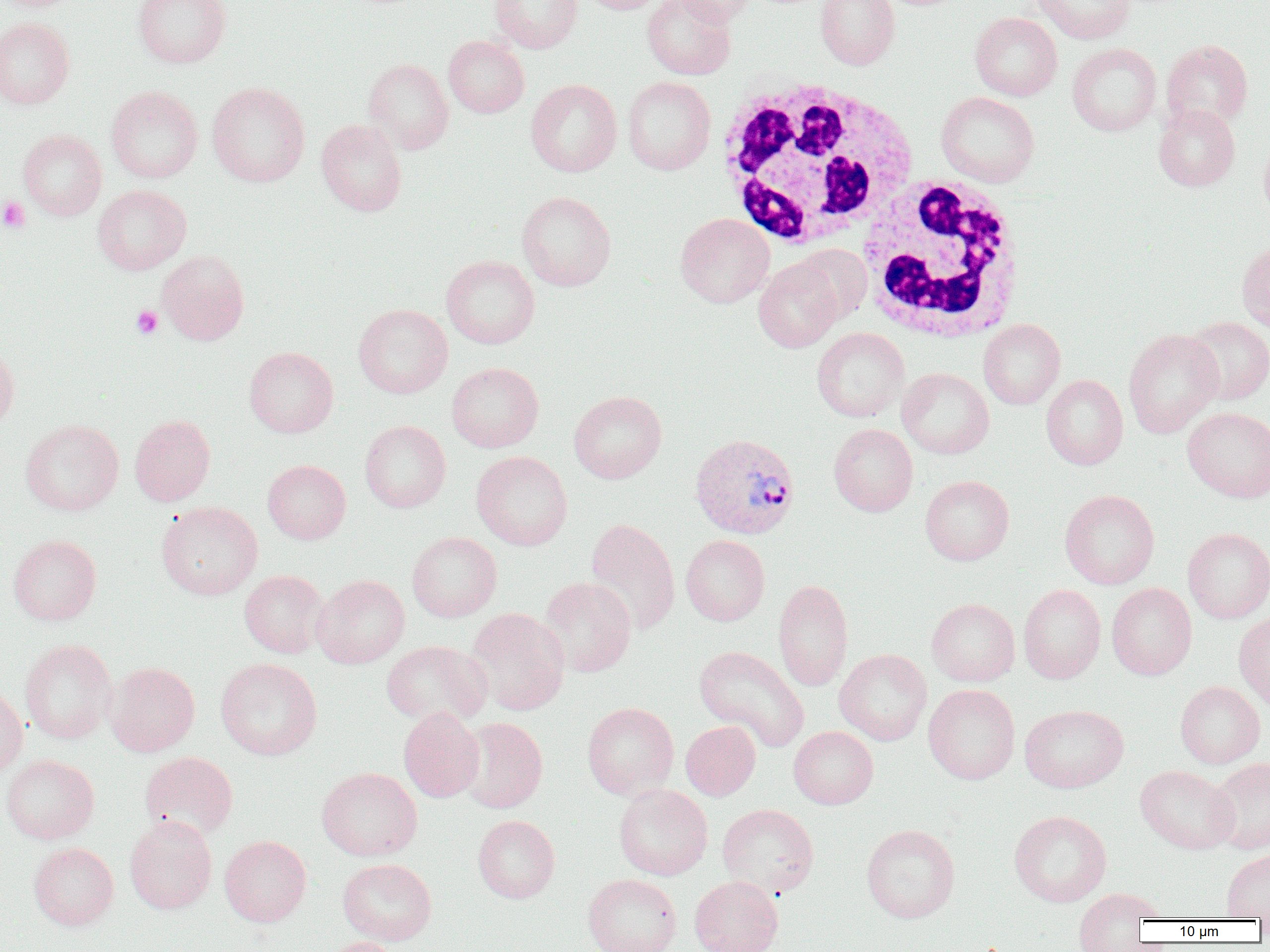

Summary:
  - Coordinate format: approximate bounding boxes as named x1/y1/x2/y2 corners in pixels
  - Platelet locations: (x1=0, y1=196, x2=31, y2=233), (x1=131, y1=305, x2=163, y2=339)
  - Plasmodium vivax-infected red blood cell locations: (x1=689, y1=433, x2=800, y2=539)
  - White blood cell locations: (x1=713, y1=77, x2=920, y2=249), (x1=855, y1=177, x2=1026, y2=343)
  - Uninfected red blood cell locations: (x1=133, y1=0, x2=231, y2=68), (x1=490, y1=0, x2=582, y2=53), (x1=579, y1=0, x2=667, y2=14), (x1=642, y1=0, x2=736, y2=80), (x1=672, y1=0, x2=757, y2=26), (x1=815, y1=0, x2=899, y2=70), (x1=1031, y1=0, x2=1134, y2=44), (x1=969, y1=12, x2=1062, y2=101), (x1=0, y1=18, x2=74, y2=109), (x1=443, y1=35, x2=529, y2=118), (x1=1161, y1=39, x2=1253, y2=131), (x1=1067, y1=43, x2=1162, y2=136), (x1=364, y1=58, x2=453, y2=154), (x1=622, y1=76, x2=716, y2=175), (x1=526, y1=79, x2=622, y2=177), (x1=207, y1=83, x2=310, y2=187), (x1=106, y1=86, x2=203, y2=183), (x1=936, y1=91, x2=1040, y2=187), (x1=1153, y1=103, x2=1240, y2=192), (x1=316, y1=119, x2=407, y2=216), (x1=18, y1=129, x2=106, y2=220), (x1=1258, y1=136, x2=1270, y2=222), (x1=92, y1=185, x2=191, y2=275), (x1=516, y1=191, x2=616, y2=291), (x1=675, y1=213, x2=774, y2=308), (x1=1237, y1=238, x2=1270, y2=334), (x1=793, y1=244, x2=872, y2=323), (x1=157, y1=250, x2=249, y2=345), (x1=441, y1=255, x2=539, y2=349), (x1=753, y1=258, x2=843, y2=352), (x1=353, y1=304, x2=452, y2=398), (x1=1183, y1=316, x2=1270, y2=405), (x1=978, y1=319, x2=1065, y2=409), (x1=812, y1=327, x2=909, y2=422), (x1=1123, y1=329, x2=1223, y2=438), (x1=0, y1=344, x2=19, y2=430), (x1=244, y1=346, x2=338, y2=437), (x1=446, y1=362, x2=544, y2=452), (x1=897, y1=367, x2=994, y2=459), (x1=1041, y1=375, x2=1128, y2=470), (x1=569, y1=390, x2=667, y2=484), (x1=1183, y1=407, x2=1270, y2=503), (x1=129, y1=414, x2=215, y2=506), (x1=20, y1=419, x2=123, y2=516), (x1=359, y1=421, x2=451, y2=513), (x1=829, y1=423, x2=918, y2=516), (x1=471, y1=451, x2=573, y2=550), (x1=262, y1=459, x2=351, y2=544), (x1=920, y1=475, x2=1014, y2=565), (x1=1059, y1=489, x2=1160, y2=589), (x1=155, y1=501, x2=262, y2=600), (x1=584, y1=518, x2=680, y2=635), (x1=1182, y1=528, x2=1270, y2=624), (x1=407, y1=531, x2=502, y2=622), (x1=8, y1=534, x2=101, y2=625), (x1=681, y1=535, x2=770, y2=626), (x1=239, y1=569, x2=328, y2=658), (x1=312, y1=574, x2=409, y2=668), (x1=539, y1=577, x2=636, y2=677), (x1=773, y1=579, x2=854, y2=691), (x1=1107, y1=583, x2=1197, y2=680), (x1=1018, y1=584, x2=1106, y2=684), (x1=926, y1=598, x2=1020, y2=686), (x1=466, y1=607, x2=569, y2=715), (x1=1234, y1=613, x2=1270, y2=712), (x1=20, y1=639, x2=117, y2=744), (x1=381, y1=640, x2=491, y2=727), (x1=694, y1=645, x2=809, y2=751), (x1=834, y1=649, x2=932, y2=745), (x1=215, y1=657, x2=322, y2=760), (x1=105, y1=662, x2=200, y2=756), (x1=1175, y1=681, x2=1265, y2=768), (x1=923, y1=683, x2=1020, y2=784), (x1=0, y1=686, x2=28, y2=778), (x1=582, y1=702, x2=679, y2=799), (x1=1019, y1=704, x2=1129, y2=793), (x1=398, y1=707, x2=484, y2=802), (x1=457, y1=717, x2=548, y2=813), (x1=680, y1=720, x2=761, y2=800), (x1=789, y1=726, x2=878, y2=809), (x1=139, y1=751, x2=238, y2=841), (x1=1, y1=754, x2=99, y2=844), (x1=1206, y1=757, x2=1270, y2=854), (x1=1135, y1=765, x2=1238, y2=854), (x1=316, y1=767, x2=422, y2=861), (x1=613, y1=783, x2=713, y2=880), (x1=717, y1=803, x2=820, y2=898), (x1=1009, y1=810, x2=1111, y2=906), (x1=124, y1=815, x2=217, y2=914), (x1=472, y1=815, x2=560, y2=903), (x1=861, y1=823, x2=960, y2=923), (x1=219, y1=835, x2=311, y2=926), (x1=28, y1=842, x2=119, y2=930), (x1=1221, y1=849, x2=1270, y2=919), (x1=338, y1=858, x2=437, y2=945), (x1=583, y1=873, x2=681, y2=952), (x1=689, y1=875, x2=783, y2=952), (x1=1073, y1=888, x2=1163, y2=947), (x1=319, y1=937, x2=408, y2=952)
  - Slide-level diagnosis: Plasmodium vivax
  - Field of view: single
  - Preparation: thin blood smear
  - Image size: 1270×952 pixels
  - Magnification: 1000x
  - Modality: light microscopy